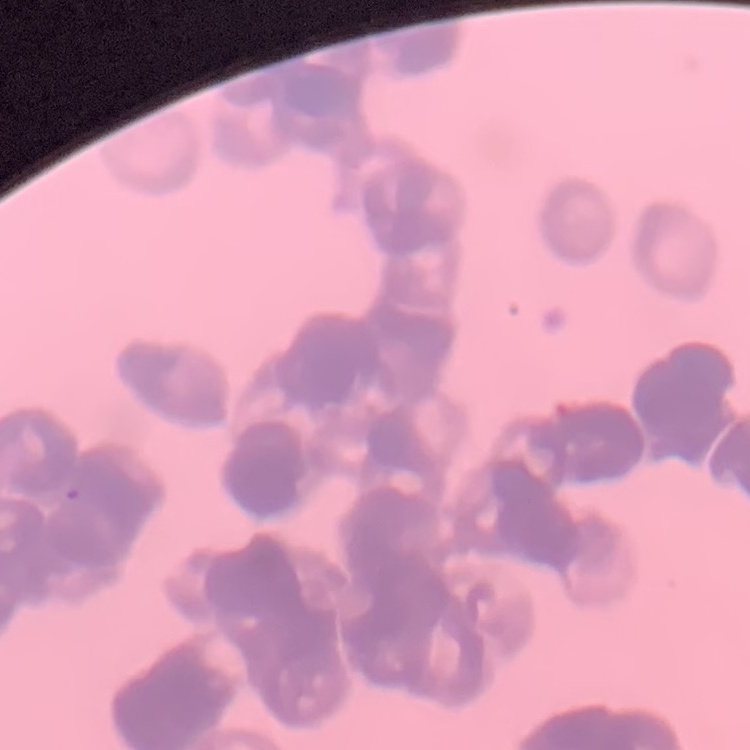

Summary:
  - Erythrocyte morphology: rouleaux formation
  - Preparation: thin blood film
  - Stain: Field's or Giemsa
  - Image type: square crop of a larger photomicrograph